Outline each blood parasite and name the species.
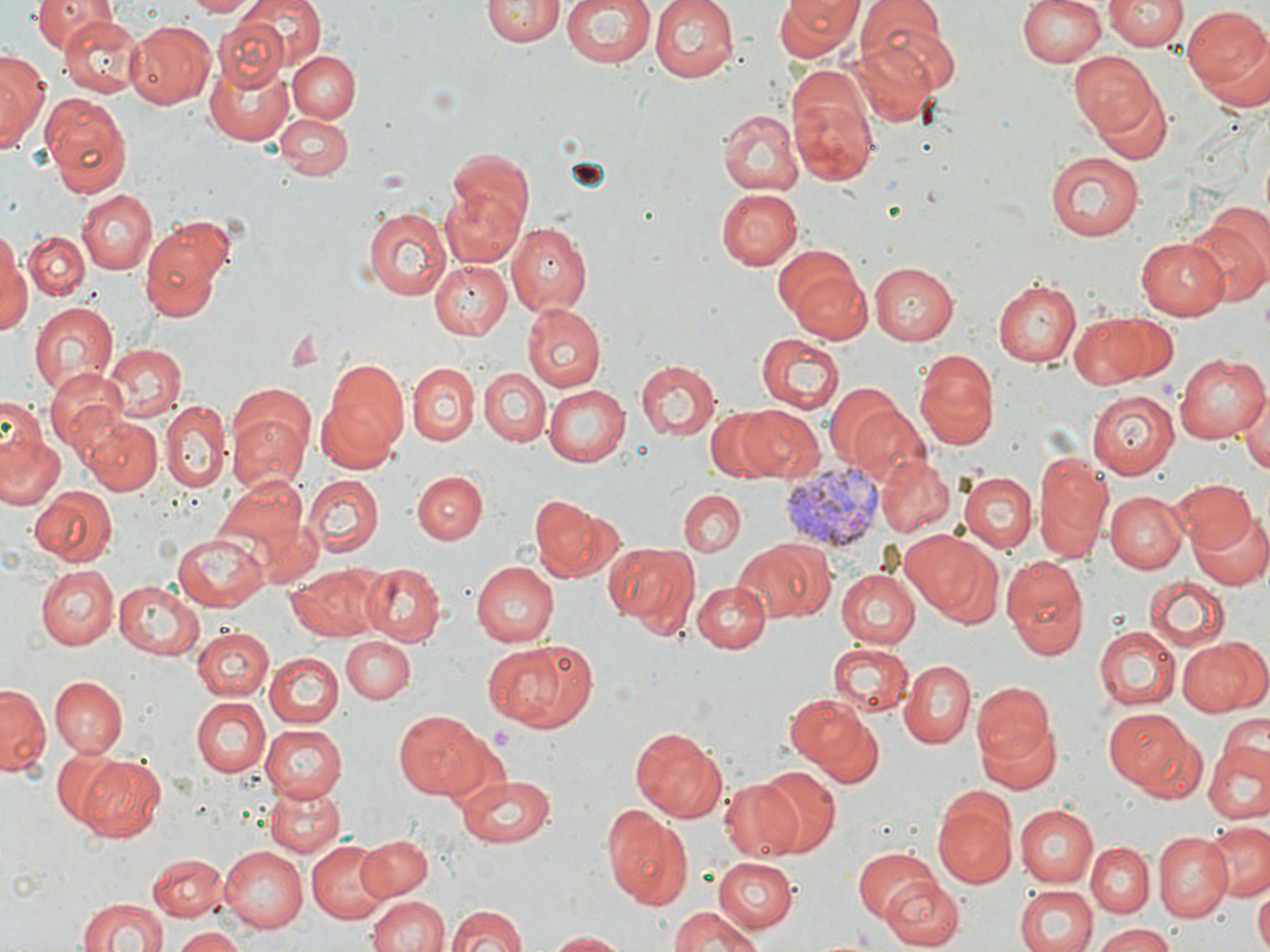
Approximate bounding boxes as (x1, y1, x2, y2) in pixels.
Plasmodium vivax-infected red blood cells: (778, 457, 887, 557).
No Plasmodium falciparum, Plasmodium ovale, Plasmodium malariae, Babesia divergens, or Trypanosoma brucei observed.

slide-level diagnosis = Plasmodium vivax
image size = 1270×952 pixels
preparation = thin blood film
uninfected red blood cell locations = approximate bounding boxes as (x1, y1, x2, y2) in pixels: (28, 0, 112, 51), (186, 0, 254, 16), (229, 0, 327, 78), (484, 0, 560, 48), (559, 0, 657, 69), (648, 0, 740, 83), (775, 0, 862, 62), (1018, 0, 1108, 68), (1105, 0, 1185, 52), (856, 1, 956, 82), (1183, 8, 1270, 104), (58, 15, 144, 97), (211, 18, 291, 92), (127, 22, 214, 108), (851, 38, 939, 127), (1069, 47, 1164, 141), (287, 50, 362, 122), (0, 52, 46, 145), (205, 56, 291, 146), (787, 72, 879, 188), (1092, 86, 1173, 165), (45, 98, 134, 195), (717, 108, 803, 196), (275, 115, 351, 180), (448, 147, 535, 236), (1045, 151, 1145, 242), (440, 187, 527, 268), (716, 187, 803, 269), (76, 188, 158, 275), (360, 206, 451, 300), (1184, 216, 1269, 309), (138, 219, 235, 320), (506, 222, 592, 316), (1, 228, 32, 338), (23, 230, 89, 300), (1137, 237, 1229, 319), (773, 245, 870, 342), (428, 259, 511, 338), (868, 262, 959, 346), (994, 279, 1081, 367), (29, 299, 118, 398), (521, 302, 605, 392), (1077, 310, 1179, 389), (755, 333, 844, 412), (105, 343, 185, 420), (913, 349, 1001, 450), (1173, 352, 1267, 444), (636, 361, 721, 442), (317, 362, 408, 470), (408, 362, 478, 446), (45, 367, 129, 453), (480, 367, 549, 447), (544, 384, 630, 464), (822, 384, 909, 467), (1240, 387, 1270, 474), (1088, 388, 1180, 480), (0, 400, 47, 468), (162, 402, 229, 495), (740, 406, 826, 483), (705, 408, 796, 481), (228, 412, 308, 493), (81, 413, 162, 496), (0, 434, 65, 509), (1033, 450, 1112, 563), (877, 455, 954, 536), (412, 470, 487, 545), (960, 471, 1035, 552), (215, 474, 310, 570), (301, 474, 383, 557), (1168, 480, 1255, 555), (31, 486, 116, 565), (677, 490, 745, 557), (1108, 490, 1188, 573), (528, 495, 616, 581), (1190, 508, 1269, 592), (906, 530, 1005, 626), (172, 532, 269, 609), (735, 540, 832, 625), (603, 541, 700, 638), (1001, 552, 1090, 660), (471, 560, 557, 646), (287, 563, 390, 643), (363, 563, 444, 647), (38, 565, 118, 650), (836, 568, 920, 648), (1143, 576, 1230, 650), (114, 580, 204, 660), (692, 580, 770, 653), (1093, 622, 1181, 711), (191, 626, 272, 700), (343, 635, 414, 706), (1178, 635, 1269, 719), (485, 640, 597, 733), (829, 642, 912, 715), (266, 651, 345, 729), (900, 660, 974, 746), (898, 669, 1050, 756), (49, 676, 126, 755), (973, 682, 1054, 765), (0, 685, 48, 776), (786, 693, 880, 781), (191, 696, 270, 778), (1102, 707, 1196, 796), (394, 711, 489, 797), (1220, 713, 1268, 767), (975, 715, 1062, 793), (260, 722, 347, 803), (630, 726, 731, 822), (1205, 741, 1270, 826), (49, 749, 131, 830), (71, 751, 166, 844), (752, 770, 843, 860), (450, 774, 558, 848), (718, 777, 805, 862), (265, 787, 344, 857), (933, 789, 1017, 890), (604, 806, 693, 907), (1014, 806, 1096, 887), (1201, 822, 1270, 901), (1155, 833, 1233, 921), (357, 835, 432, 899), (306, 841, 390, 923), (1087, 843, 1153, 917), (219, 846, 307, 933), (852, 846, 941, 925), (146, 854, 225, 922), (712, 858, 796, 932), (882, 873, 965, 947), (1014, 885, 1098, 952), (1253, 887, 1270, 952), (364, 894, 447, 952), (76, 896, 166, 952), (442, 904, 530, 952), (667, 909, 765, 952), (1091, 925, 1179, 952), (169, 927, 244, 952), (543, 930, 629, 951)
magnification = 1000x
field of view = one of a larger specimen
modality = light microscopy
stain = May-Grünwald-Giemsa